Report the malaria status of this cell.
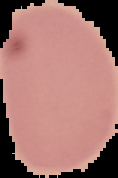

Uninfected.

Summary:
  - Image size: 118×178 pixels
  - Preparation: thin blood film
  - Image type: segmented cell region with the area outside set to black